Outline each uninfected red blood cell.
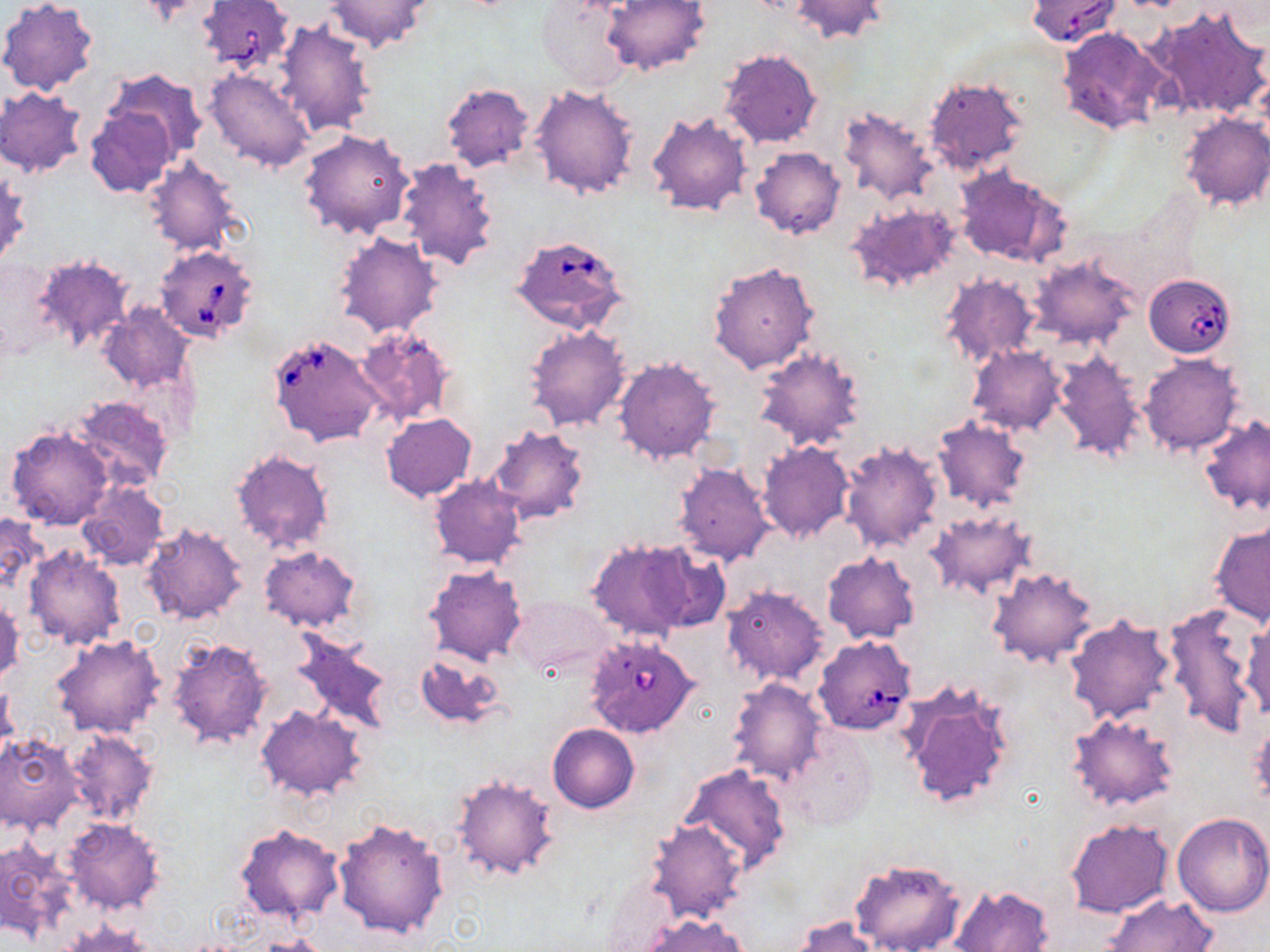
Approximate bounding boxes as (x1,y1)-(x2,y2) corner pairs in pixels.
Uninfected red blood cells: (0,0)-(98,96), (326,0)-(433,53), (602,0)-(710,75), (788,0)-(890,43), (537,2)-(633,94), (1148,5)-(1270,121), (273,18)-(378,137), (1056,26)-(1168,135), (719,47)-(823,147), (103,68)-(209,163), (205,68)-(317,173), (923,77)-(1029,175), (440,82)-(536,172), (529,82)-(640,201), (0,88)-(86,177), (86,104)-(177,196), (836,106)-(939,205), (644,110)-(751,218), (1179,113)-(1270,212), (298,128)-(415,241), (750,147)-(845,240), (142,156)-(243,257), (395,156)-(501,271), (1,163)-(29,269), (952,165)-(1069,268), (846,202)-(963,295), (332,230)-(444,338), (33,254)-(134,355), (1029,255)-(1140,350), (705,260)-(819,375), (940,275)-(1042,368), (98,304)-(195,394), (524,324)-(632,431), (355,327)-(457,425), (753,344)-(866,452), (968,345)-(1067,436), (1050,350)-(1147,464), (611,355)-(722,465), (1140,355)-(1244,457), (69,397)-(175,493), (381,413)-(476,501), (931,415)-(1032,513), (1199,415)-(1269,516), (488,425)-(593,526), (6,426)-(114,531), (756,442)-(854,544), (840,442)-(943,554), (231,449)-(333,554), (671,462)-(776,567), (428,475)-(526,570), (77,482)-(168,571), (925,508)-(1037,600), (0,511)-(45,597), (141,522)-(249,626), (1209,523)-(1269,626), (585,539)-(696,641), (639,542)-(731,633), (22,546)-(126,651), (260,546)-(361,631), (821,551)-(921,644), (424,565)-(526,666), (987,567)-(1098,667), (721,584)-(831,686), (507,594)-(613,678), (1,597)-(24,687), (1163,605)-(1264,738), (1063,614)-(1177,726), (1241,618)-(1270,720), (290,632)-(395,734), (52,635)-(163,739), (166,636)-(272,748), (415,651)-(507,730), (726,676)-(829,783), (897,678)-(1017,812), (0,683)-(19,765), (256,705)-(367,801), (1065,712)-(1180,813), (547,722)-(639,814), (1249,723)-(1270,809), (781,726)-(877,830), (64,729)-(157,824), (0,734)-(82,834), (679,763)-(791,874), (451,774)-(560,881), (1171,812)-(1270,917), (333,815)-(449,940), (646,816)-(749,923), (63,818)-(164,914), (1065,818)-(1174,918), (234,823)-(343,923), (0,839)-(74,941), (850,857)-(966,952), (950,884)-(1054,952), (1101,893)-(1219,952), (638,914)-(748,952), (792,917)-(879,952), (60,921)-(157,951), (252,935)-(334,952).

Summary:
  - Babesia divergens-infected red blood cell locations: (197,0)-(294,73), (1026,0)-(1122,47), (511,233)-(631,335), (155,244)-(259,344), (1143,273)-(1237,357), (270,333)-(384,446), (585,634)-(702,739), (814,636)-(916,736)
  - Slide-level diagnosis: Babesia divergens
  - Preparation: thin blood film
  - Stain: May-Grünwald-Giemsa
  - Magnification: 1000x
  - Field of view: single
  - Image size: 1270×952 pixels
  - Modality: light microscopy